Name the parasite shown.
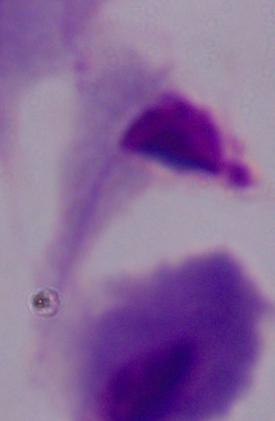

A trichomonad.

Captured at 1000x magnification. Photomicrograph.